Assess this cell for malaria.
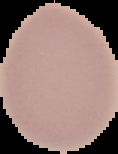
Uninfected.

Summary:
  - Image type: cell region segmented out of the field of view; surrounding area masked to black
  - Image size: 118×154 pixels
  - Preparation: thin blood film